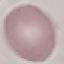

malaria status = uninfected
image type = automatically extracted cell patch, resized to 64 × 64 pixels
stain = Giemsa
preparation = thin blood film
capture = smartphone camera at the microscope eyepiece